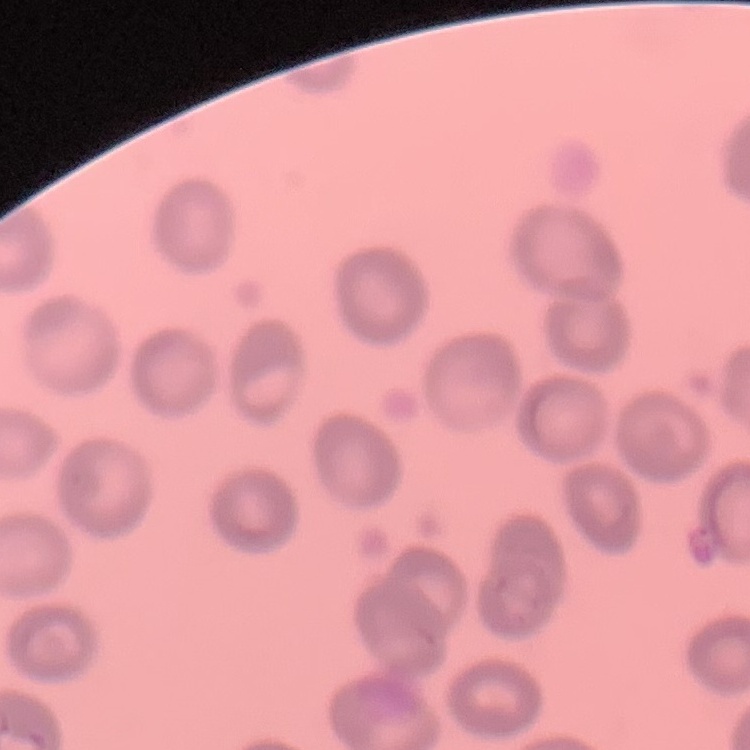

Summary:
  - Erythrocyte morphology: no rouleaux formation
  - Image type: square crop of a larger photomicrograph
  - Preparation: thin peripheral smear
  - Stain: Field's or Giemsa